Report the malaria status of this cell.
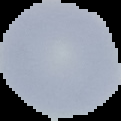

Uninfected.

image_size: 121×121 pixels
image_type: segmented cell region with the area outside set to black
preparation: thin blood film